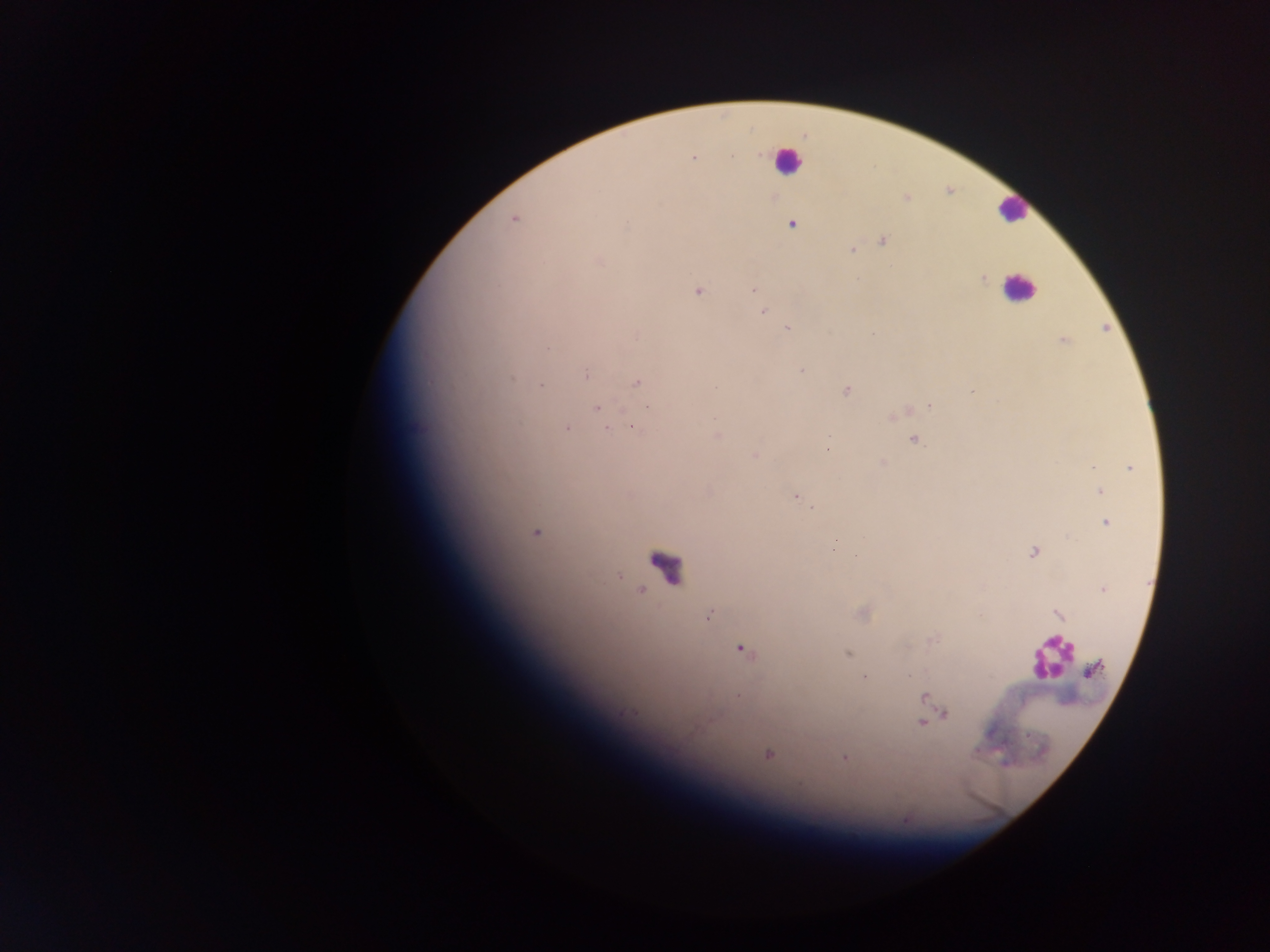
Approximate centers as (x, y) in pixels. Plasmodium parasite locations: (760, 154), (732, 156), (693, 158), (906, 198), (513, 220), (627, 225), (792, 225), (884, 241), (852, 250), (598, 261), (857, 279), (983, 279), (754, 289), (697, 291), (763, 311), (788, 328), (872, 334), (1063, 341), (548, 348), (801, 371), (586, 374), (512, 379), (637, 382), (540, 386), (847, 391), (930, 406), (597, 407), (633, 427), (566, 428), (607, 430), (717, 436), (914, 440), (827, 450), (755, 455), (883, 462), (1093, 467), (1129, 468), (1100, 491), (795, 497), (812, 508), (1106, 522), (535, 533), (834, 544), (1034, 552), (856, 556), (1103, 589), (1058, 614), (709, 615), (934, 639), (743, 650), (847, 653), (1093, 669), (909, 675), (865, 677), (737, 696), (925, 696), (945, 714), (921, 723), (768, 754), (845, 757). Leukocyte locations: (787, 160), (1013, 209), (1018, 288), (662, 565), (1050, 657). Collected in Ghana. Thick blood smear. One field of view. Photographed through a microscope with a mobile-phone camera. Image is 1270×952 pixels.